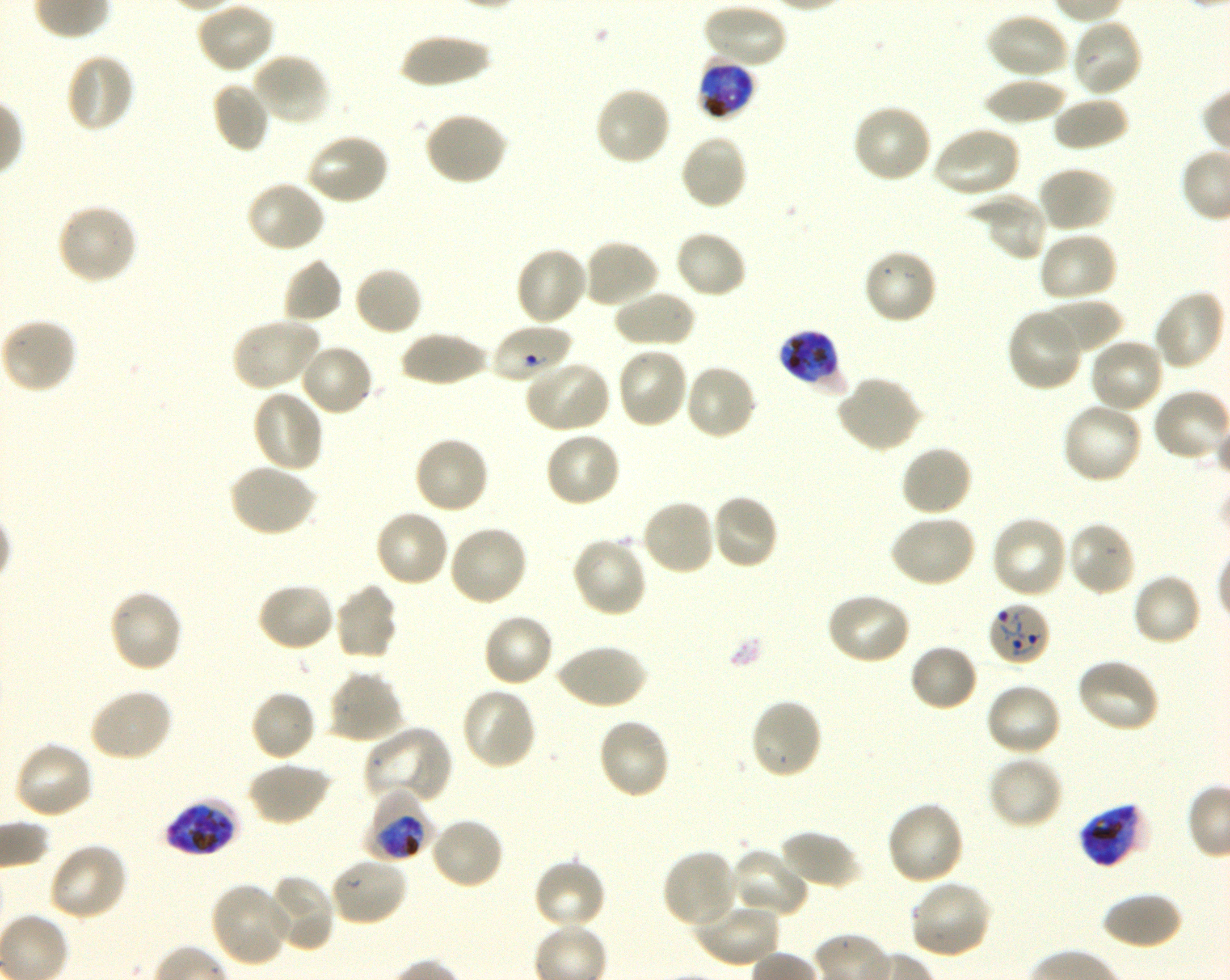

Not every red blood cell is marked. A life-cycle stage — or a range of stages, where the recorded stages span more than one — follows each staged infected red blood cell.
locations of infected red blood cells = approximate bounding boxes as [x1, y1, x2, y2] in pixels: [698, 59, 756, 120] late trophozoite to early schizont; [777, 329, 845, 393] early trophozoite to early schizont; [988, 601, 1051, 667] ring; [365, 790, 431, 864] trophozoite; [163, 798, 240, 858] late trophozoite to late schizont; [1078, 801, 1152, 868] late trophozoite to late schizont
life-cycle stages observed = ring, trophozoite
culture = in-vitro P. falciparum strain 3D7, shaking
locations of uninfected red blood cells = approximate bounding boxes as [x1, y1, x2, y2] in pixels: [194, 0, 276, 75], [701, 2, 788, 70], [985, 12, 1069, 80], [1069, 16, 1144, 97], [397, 32, 493, 87], [64, 51, 137, 134], [250, 52, 331, 127], [981, 77, 1070, 125], [211, 81, 271, 154], [593, 85, 672, 166], [1052, 95, 1129, 152], [851, 102, 934, 184], [423, 111, 509, 187], [931, 126, 1021, 198], [305, 131, 392, 207], [678, 132, 749, 211], [1036, 165, 1116, 234], [245, 180, 327, 255], [969, 192, 1050, 263], [55, 203, 139, 285], [674, 230, 748, 300], [1037, 231, 1119, 304], [581, 238, 661, 310], [514, 246, 589, 327], [861, 247, 938, 325], [282, 257, 342, 324], [353, 265, 424, 337], [1152, 289, 1227, 372], [611, 291, 696, 348], [1040, 296, 1123, 356], [1006, 307, 1085, 393], [1, 317, 78, 395], [230, 317, 321, 393], [399, 331, 491, 387], [1087, 336, 1166, 415], [299, 342, 375, 417], [615, 346, 690, 429], [522, 359, 611, 434], [683, 363, 758, 441], [836, 375, 922, 454], [251, 389, 326, 473], [1060, 402, 1144, 485], [543, 431, 622, 508], [412, 435, 491, 515], [899, 444, 973, 518], [227, 464, 317, 538], [709, 493, 779, 571], [640, 498, 716, 577], [373, 508, 451, 588], [889, 514, 977, 588], [990, 514, 1070, 600], [1066, 520, 1137, 596], [447, 524, 530, 608], [570, 536, 649, 618], [1130, 573, 1202, 648], [256, 581, 337, 652], [333, 583, 400, 661], [108, 589, 183, 674], [825, 591, 911, 666], [482, 612, 555, 689], [555, 642, 647, 710], [908, 643, 979, 713], [1074, 658, 1161, 734], [327, 670, 406, 744], [984, 682, 1063, 758], [87, 686, 174, 763], [461, 687, 537, 770], [249, 689, 317, 763], [749, 698, 824, 781], [596, 717, 671, 800], [362, 725, 454, 805], [12, 739, 95, 820], [987, 754, 1064, 830], [245, 760, 331, 826], [885, 801, 966, 887], [429, 816, 505, 891], [778, 829, 861, 892], [48, 842, 129, 922], [729, 847, 809, 919], [661, 848, 739, 930], [327, 856, 408, 928], [531, 858, 608, 933], [264, 874, 336, 952], [909, 879, 994, 960], [208, 882, 294, 967], [1101, 890, 1183, 950], [691, 899, 780, 967]
preparation = thin blood smear
field of view = single
donor blood group = O+
stain = Giemsa
locations of red blood cells of indeterminate infection status = approximate bounding boxes as [x1, y1, x2, y2] in pixels: [491, 323, 573, 384]
image size = 1230×980 pixels
objective = 100x, oil immersion, numerical aperture 1.30